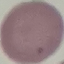
{
  "result": "negative for malaria parasites",
  "preparation": "thin blood film",
  "capture": "smartphone camera at the microscope eyepiece",
  "image_type": "cell patch, automatically extracted from a larger field of view and resized to 64 × 64 pixels",
  "stain": "Giemsa"
}